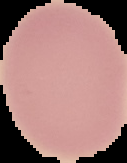

Image is 127×163 pixels. Result: negative for malaria parasites. Cell region segmented out of the field of view; the surrounding area is masked to black. From a thin blood smear.